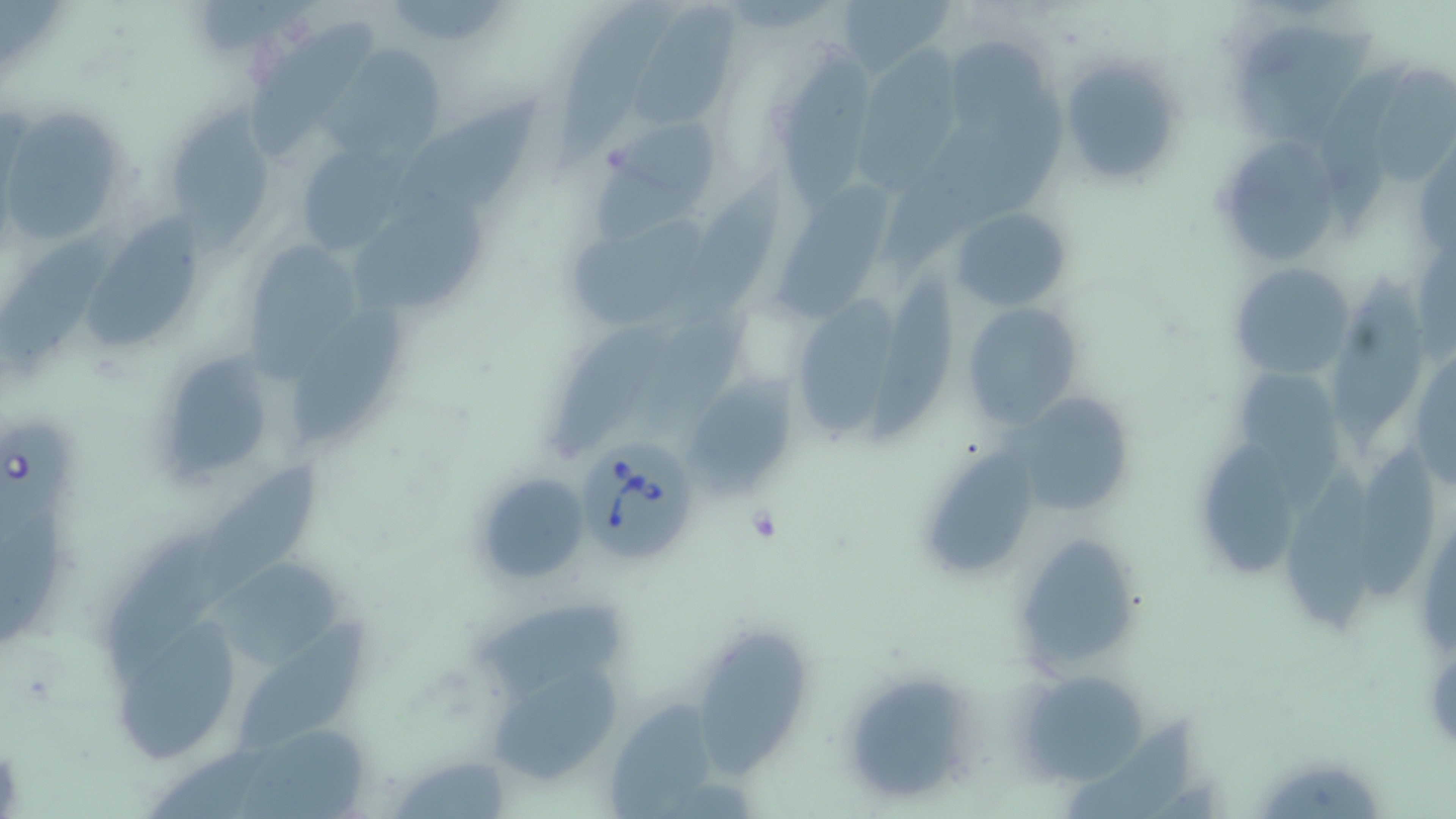
Summary:
  - Coordinate format: approximate bounding boxes as (x1, y1, x2, y2) in pixels
  - Uninfected red blood cell locations: (554, 0, 688, 169), (835, 0, 952, 82), (631, 4, 741, 130), (249, 19, 387, 157), (1235, 25, 1378, 147), (952, 33, 1070, 146), (327, 41, 453, 161), (853, 46, 985, 194), (776, 50, 881, 213), (1325, 55, 1408, 235), (1063, 56, 1184, 189), (1371, 63, 1455, 181), (394, 95, 547, 218), (0, 106, 128, 247), (164, 106, 280, 261), (587, 117, 720, 239), (1217, 138, 1342, 264), (291, 140, 416, 258), (772, 176, 900, 326), (666, 182, 788, 330), (353, 198, 500, 316), (951, 206, 1071, 311), (79, 213, 216, 357), (559, 216, 712, 330), (0, 221, 129, 382), (247, 244, 363, 385), (1228, 262, 1354, 379), (873, 265, 960, 445), (1331, 273, 1430, 449), (799, 296, 913, 441), (960, 301, 1086, 428), (634, 310, 752, 441), (298, 314, 418, 444), (558, 323, 670, 458), (1410, 343, 1455, 491), (161, 350, 265, 481), (1240, 369, 1353, 513), (686, 383, 800, 500), (1026, 398, 1137, 516), (1200, 438, 1304, 576), (928, 442, 1040, 580), (1359, 448, 1444, 605), (1283, 460, 1386, 637), (189, 461, 330, 605), (472, 470, 593, 588), (99, 531, 222, 682), (1016, 541, 1142, 666), (201, 560, 350, 676), (480, 599, 629, 702), (113, 606, 244, 764), (243, 619, 367, 752), (697, 631, 816, 782), (480, 664, 626, 786), (1013, 670, 1150, 785), (846, 673, 972, 804), (610, 688, 725, 819), (1064, 717, 1201, 819), (232, 720, 381, 819), (1262, 759, 1385, 819)
  - Babesia divergens-infected red blood cell locations: (1, 412, 76, 546), (576, 446, 702, 566)
  - Slide-level diagnosis: Babesia divergens
  - Stain: May-Grünwald-Giemsa
  - Modality: optical microscopy
  - Field of view: single
  - Magnification: 1000x
  - Image size: 1456×819 pixels
  - Preparation: thin blood smear